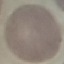

Result: no malaria parasites seen. Thin blood smear. Giemsa stain. Acquired by smartphone through the microscope eyepiece. Automatically extracted cell patch, resized to 64 × 64 pixels.